Name the blood parasite species.
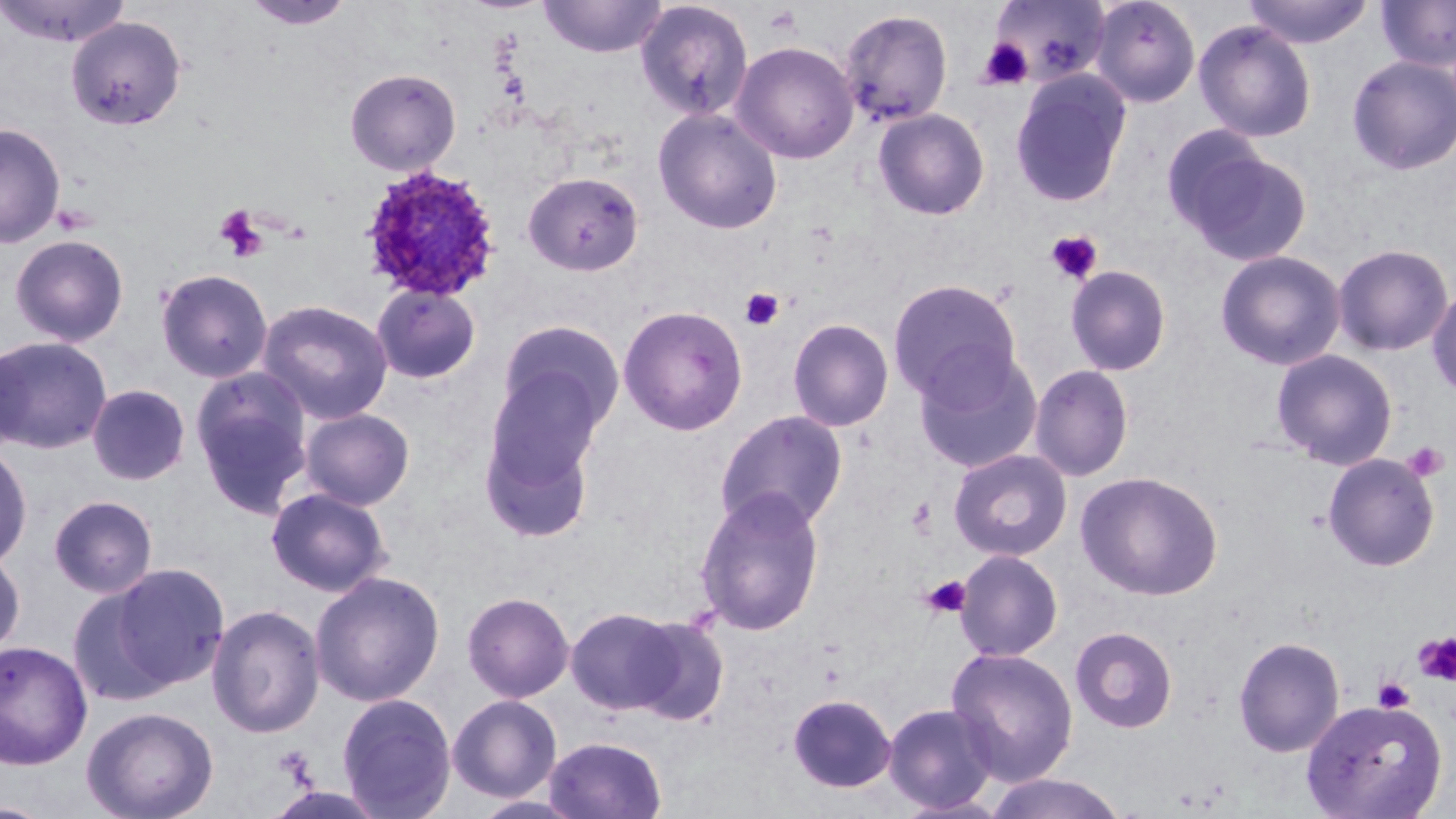

Plasmodium ovale.

Summary:
  - Coordinate format: approximate bounding boxes as (x1, y1, x2, y2) in pixels
  - Uninfected red blood cell locations: (1, 0, 131, 48), (539, 0, 667, 58), (1089, 0, 1201, 107), (1242, 0, 1374, 49), (1376, 0, 1456, 72), (241, 1, 356, 31), (635, 1, 754, 121), (992, 1, 1112, 86), (839, 8, 953, 128), (65, 15, 187, 131), (1193, 20, 1317, 142), (731, 41, 859, 163), (1346, 54, 1456, 176), (344, 67, 462, 176), (1010, 71, 1131, 208), (653, 107, 783, 234), (873, 108, 990, 220), (0, 122, 66, 249), (1170, 136, 1312, 266), (522, 171, 645, 276), (9, 233, 130, 346), (1333, 243, 1453, 357), (1215, 250, 1347, 371), (1065, 265, 1172, 376), (155, 268, 273, 383), (887, 278, 1023, 404), (370, 282, 481, 385), (1426, 283, 1456, 401), (257, 298, 394, 424), (618, 305, 748, 436), (788, 318, 894, 432), (497, 320, 624, 435), (1, 335, 112, 454), (0, 343, 27, 454), (913, 348, 1044, 474), (1271, 349, 1398, 470), (1029, 364, 1134, 482), (189, 367, 315, 516), (87, 383, 190, 485), (482, 388, 604, 540), (299, 408, 415, 509), (715, 410, 849, 532), (0, 441, 34, 570), (948, 449, 1072, 562), (1322, 453, 1440, 572), (1076, 471, 1224, 601), (265, 486, 393, 597), (693, 486, 826, 637), (48, 494, 158, 598), (954, 550, 1063, 661), (0, 551, 26, 660), (108, 563, 230, 689), (309, 570, 445, 707), (67, 585, 175, 706), (462, 591, 574, 702), (206, 603, 325, 738), (565, 606, 684, 715), (628, 615, 729, 725), (1069, 626, 1178, 733), (1233, 635, 1345, 757), (0, 640, 93, 770), (945, 646, 1079, 786), (336, 692, 457, 818), (787, 693, 896, 793), (447, 694, 562, 802), (1300, 698, 1447, 818), (882, 702, 1000, 815), (80, 706, 219, 819), (543, 735, 667, 819), (270, 743, 318, 788), (981, 772, 1130, 819), (469, 794, 589, 819)
  - Platelet locations: (763, 6, 802, 36), (979, 37, 1033, 91), (214, 204, 268, 261), (1045, 231, 1103, 284), (740, 288, 785, 331), (1403, 441, 1449, 483), (921, 575, 972, 618), (1414, 632, 1456, 686), (1373, 677, 1414, 713), (272, 745, 316, 784)
  - Plasmodium ovale-infected red blood cell locations: (358, 164, 504, 304)
  - Modality: optical microscopy
  - Magnification: 1000x
  - Image size: 1456×819 pixels
  - Preparation: thin blood smear
  - Field of view: single
  - Stain: May-Grünwald-Giemsa